Assess this cell for malaria.
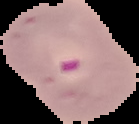

Parasitized.

Segmented cell region on a black background. From a thin blood film. Image is 139×124 pixels.